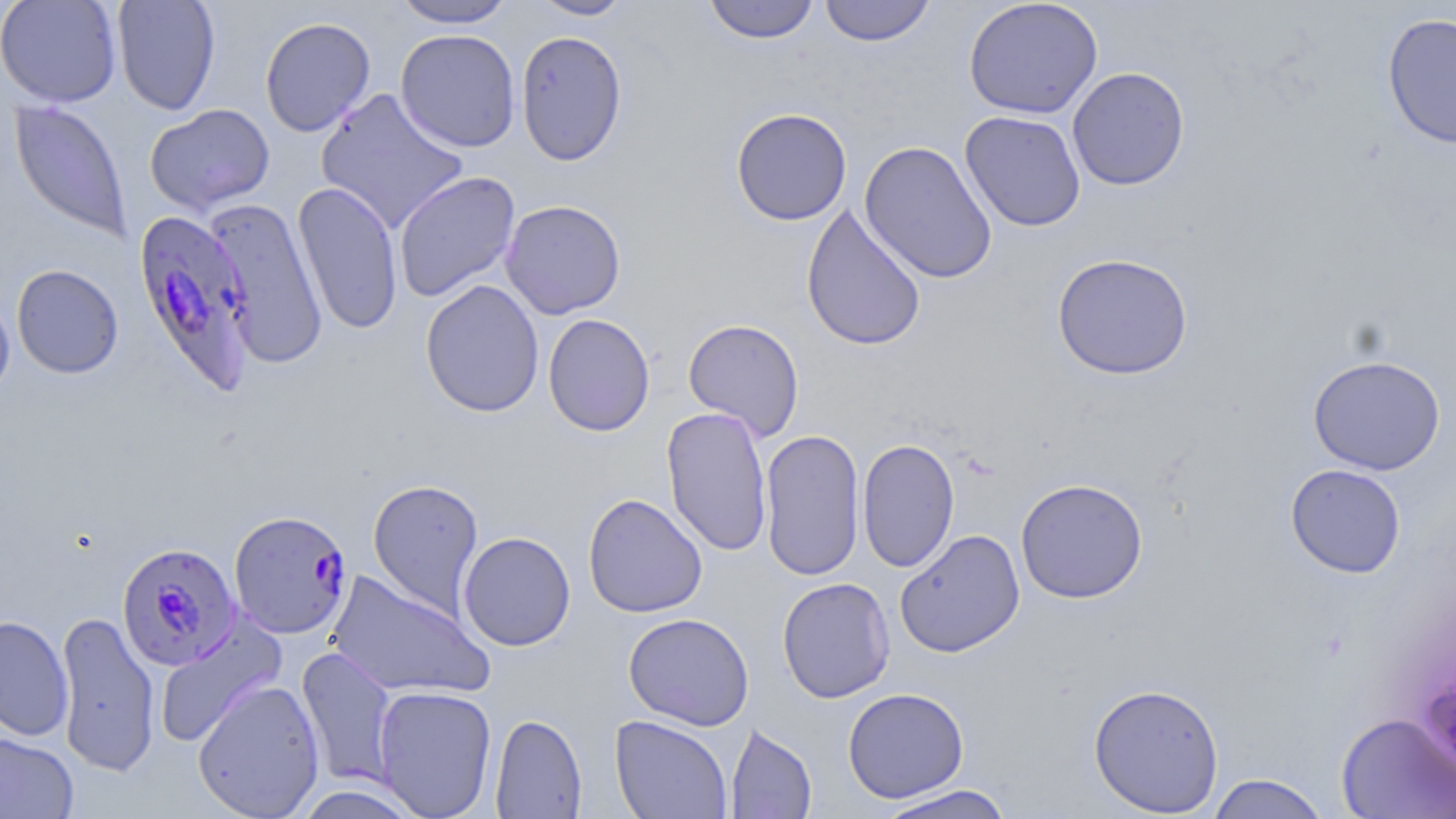

Summary:
  - Coordinate format: approximate bounding boxes as named x1/y1/x2/y2 corners in pixels
  - Plasmodium falciparum-infected red blood cell locations: (x1=133, y1=208, x2=255, y2=392), (x1=229, y1=509, x2=353, y2=641), (x1=117, y1=542, x2=242, y2=671)
  - Uninfected red blood cell locations: (x1=0, y1=0, x2=122, y2=108), (x1=112, y1=0, x2=221, y2=115), (x1=391, y1=0, x2=517, y2=29), (x1=530, y1=0, x2=634, y2=20), (x1=703, y1=0, x2=820, y2=44), (x1=819, y1=0, x2=936, y2=46), (x1=964, y1=0, x2=1103, y2=120), (x1=1382, y1=12, x2=1456, y2=150), (x1=259, y1=16, x2=376, y2=137), (x1=395, y1=29, x2=521, y2=152), (x1=515, y1=30, x2=628, y2=166), (x1=1067, y1=67, x2=1190, y2=190), (x1=314, y1=87, x2=469, y2=235), (x1=9, y1=99, x2=133, y2=242), (x1=144, y1=103, x2=275, y2=216), (x1=731, y1=107, x2=852, y2=225), (x1=959, y1=111, x2=1086, y2=232), (x1=858, y1=140, x2=997, y2=284), (x1=394, y1=171, x2=521, y2=303), (x1=292, y1=181, x2=404, y2=336), (x1=204, y1=197, x2=329, y2=369), (x1=500, y1=199, x2=626, y2=319), (x1=801, y1=202, x2=926, y2=351), (x1=1052, y1=252, x2=1193, y2=380), (x1=11, y1=264, x2=124, y2=379), (x1=420, y1=279, x2=545, y2=418), (x1=0, y1=290, x2=15, y2=405), (x1=543, y1=313, x2=655, y2=436), (x1=683, y1=318, x2=804, y2=441), (x1=1307, y1=355, x2=1446, y2=476), (x1=662, y1=405, x2=773, y2=557), (x1=759, y1=428, x2=865, y2=581), (x1=857, y1=438, x2=959, y2=573), (x1=1285, y1=463, x2=1406, y2=578), (x1=367, y1=478, x2=484, y2=617), (x1=1015, y1=478, x2=1148, y2=604), (x1=583, y1=493, x2=707, y2=618), (x1=895, y1=529, x2=1025, y2=657), (x1=458, y1=531, x2=576, y2=651), (x1=326, y1=569, x2=494, y2=701), (x1=777, y1=577, x2=895, y2=703), (x1=54, y1=610, x2=161, y2=778), (x1=623, y1=612, x2=755, y2=730), (x1=0, y1=615, x2=74, y2=741), (x1=154, y1=618, x2=285, y2=748), (x1=296, y1=646, x2=398, y2=787), (x1=191, y1=678, x2=326, y2=819), (x1=1088, y1=681, x2=1225, y2=816), (x1=372, y1=685, x2=497, y2=818), (x1=842, y1=687, x2=969, y2=803), (x1=1336, y1=712, x2=1456, y2=818), (x1=490, y1=713, x2=587, y2=819), (x1=610, y1=715, x2=733, y2=818), (x1=726, y1=723, x2=817, y2=819), (x1=0, y1=731, x2=79, y2=818), (x1=1206, y1=773, x2=1330, y2=819), (x1=873, y1=784, x2=1017, y2=819), (x1=291, y1=785, x2=424, y2=819)
  - Slide-level diagnosis: Plasmodium falciparum
  - Preparation: thin blood smear
  - Stain: May-Grünwald-Giemsa
  - Field of view: single
  - Magnification: 1000x
  - Modality: light microscopy
  - Image size: 1456×819 pixels